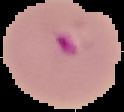
Summary:
  - Image size: 124×112 pixels
  - Preparation: thin blood film
  - Image type: segmented cell region with the area outside set to black
  - Result: Plasmodium parasites detected